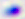
magnification: 400x
modality: micrograph
identification: Toxoplasma gondii